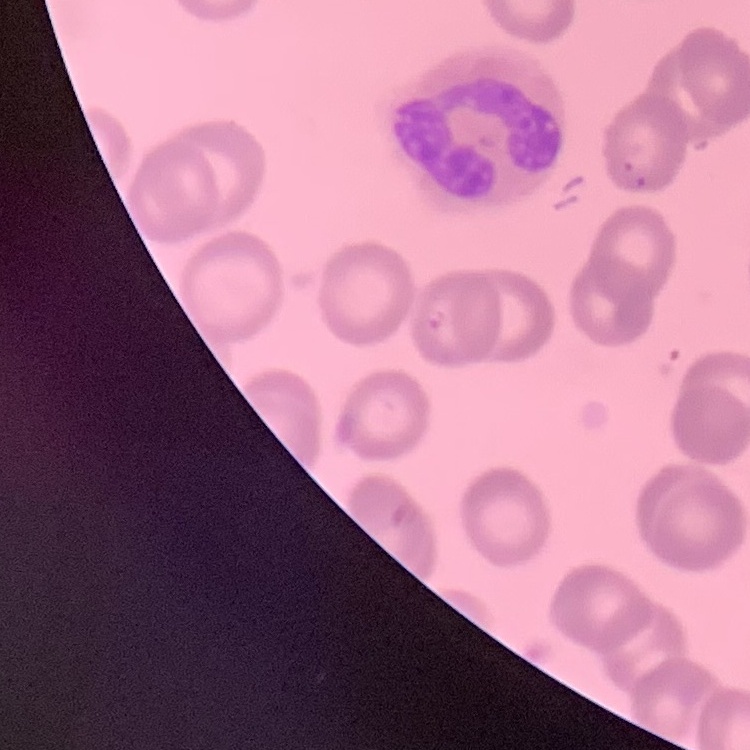

The erythrocytes show no rouleaux formation. Square crop of a larger photomicrograph. Field's or Giemsa stain. Thin blood smear.